Identify the cell.
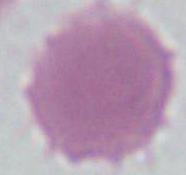

An erythrocyte.

Summary:
  - Magnification: 1000x
  - Modality: photomicrograph